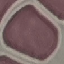
Result: negative for malaria parasites. Photographed with a smartphone camera at the microscope eyepiece. Automatically extracted cell patch, resized to 64 × 64 pixels. Giemsa-stained preparation. Thin smear of blood.